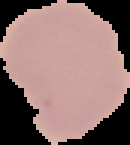

From a thin blood film. Cell region segmented out of the field of view; the surrounding area is masked to black. Image is 130×145 pixels. Malaria status: uninfected.